Assess for Plasmodium parasites.
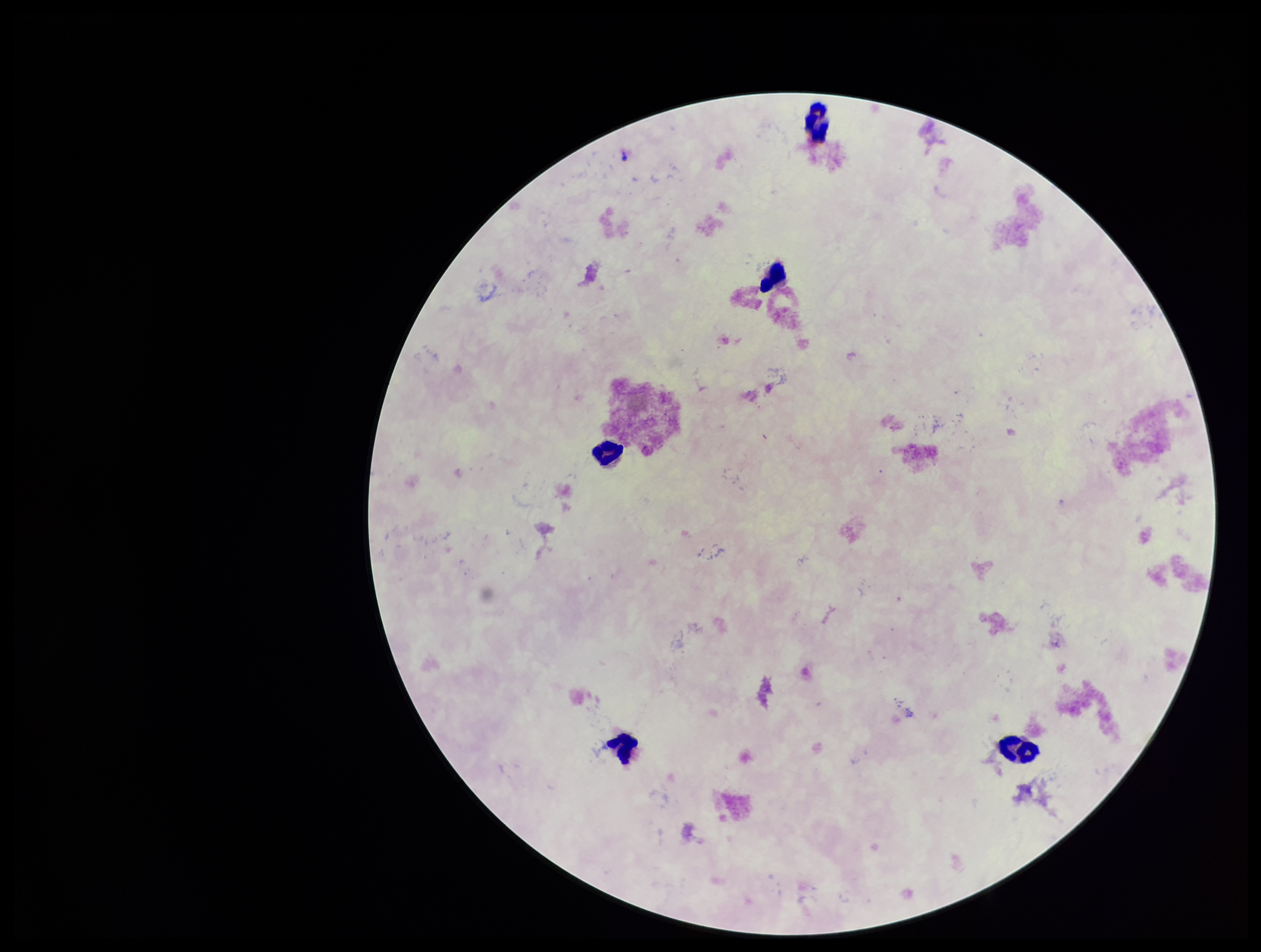
None detected.

Parasite count: 0. Leukocyte count: 5. Image is 1261×952 pixels. Single field of view. Patient malaria status: negative. Preparation: thick smear. Stained with Giemsa. Smartphone photograph taken through the eyepiece of a microscope.